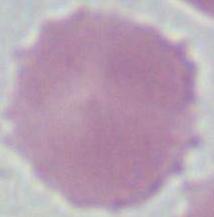
modality = photomicrograph
identification = red blood cell
magnification = 1000x